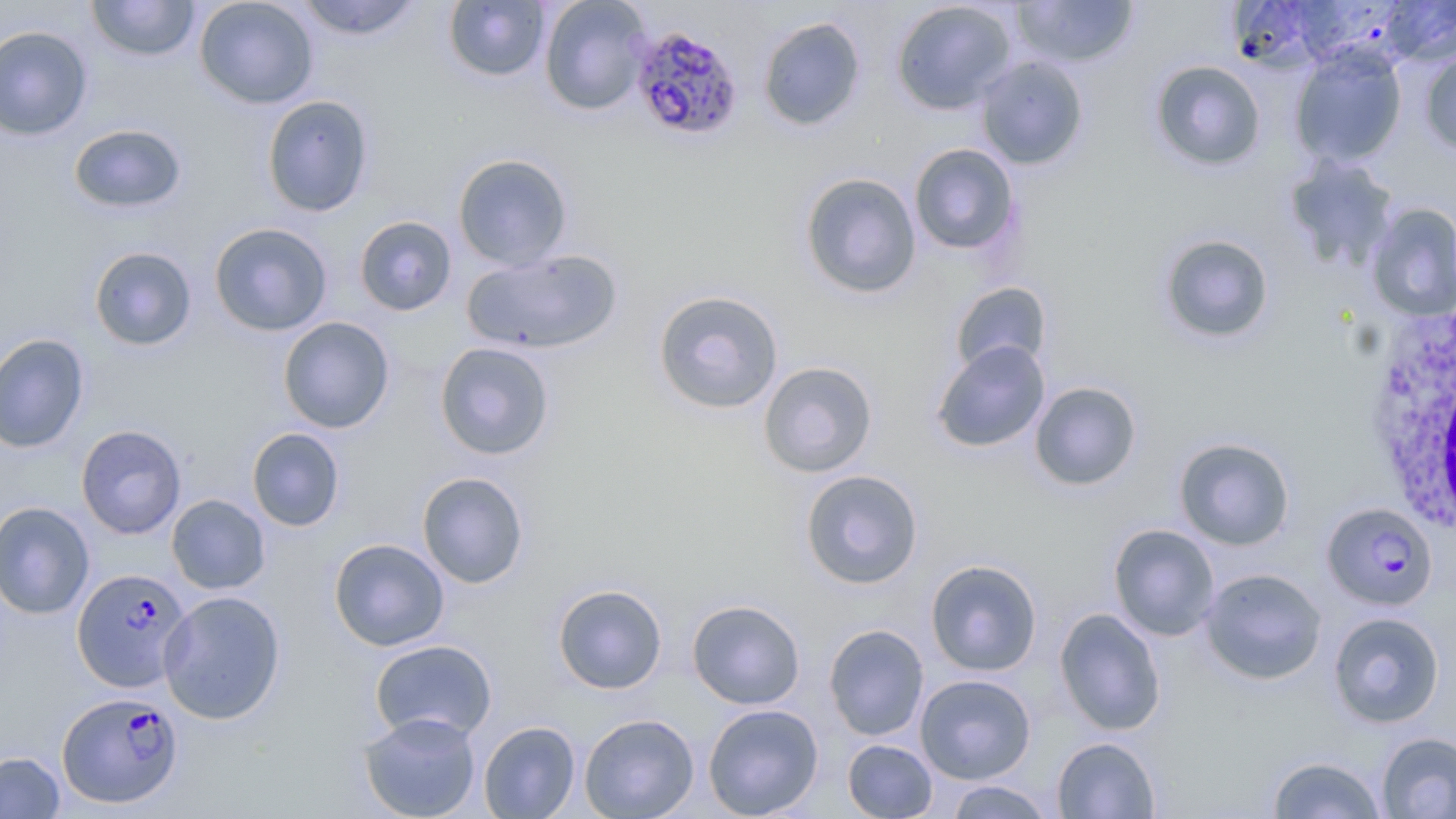

Summary:
  - Coordinate format: approximate bounding boxes as (x1, y1, x2, y2) in pixels
  - White blood cell locations: (1364, 301, 1456, 532)
  - Uninfected red blood cell locations: (86, 0, 201, 62), (194, 0, 319, 109), (294, 0, 424, 41), (539, 0, 653, 115), (1011, 0, 1140, 69), (1226, 0, 1344, 74), (1381, 0, 1456, 67), (443, 1, 550, 82), (890, 1, 1017, 115), (757, 16, 866, 132), (0, 25, 94, 141), (1290, 45, 1407, 168), (1419, 50, 1456, 155), (975, 55, 1089, 170), (1149, 60, 1267, 172), (261, 95, 375, 217), (68, 123, 187, 214), (908, 143, 1020, 256), (452, 153, 573, 271), (1283, 155, 1400, 271), (799, 172, 922, 299), (1366, 203, 1456, 321), (354, 215, 457, 316), (209, 222, 333, 336), (1157, 233, 1275, 345), (88, 246, 197, 351), (461, 248, 623, 355), (950, 281, 1052, 376), (653, 289, 784, 415), (278, 316, 395, 433), (0, 332, 90, 454), (931, 340, 1050, 454), (434, 341, 555, 460), (757, 361, 878, 478), (1029, 381, 1142, 491), (76, 425, 186, 539), (246, 427, 345, 532), (1173, 436, 1295, 550), (799, 469, 924, 589), (416, 471, 529, 589), (166, 494, 270, 594), (0, 501, 95, 619), (1108, 523, 1221, 641), (329, 538, 449, 651), (925, 558, 1043, 677), (1200, 568, 1327, 685), (552, 583, 668, 694), (158, 590, 286, 725), (687, 599, 805, 710), (1053, 607, 1166, 735), (1328, 611, 1444, 728), (824, 624, 929, 740), (369, 639, 498, 742), (915, 673, 1037, 784), (703, 703, 823, 818), (358, 711, 482, 819), (579, 713, 700, 819), (478, 720, 581, 818), (1376, 732, 1456, 818), (1052, 737, 1160, 819), (842, 739, 937, 818), (0, 751, 65, 818), (1266, 755, 1387, 818), (944, 780, 1055, 818)
  - Plasmodium falciparum-infected red blood cell locations: (631, 25, 745, 142), (1322, 502, 1438, 612), (72, 568, 192, 692), (57, 691, 182, 808)
  - Slide-level diagnosis: Plasmodium falciparum
  - Image size: 1456×819 pixels
  - Field of view: single
  - Modality: optical microscopy
  - Stain: May-Grünwald-Giemsa
  - Magnification: 1000x
  - Preparation: thin blood smear